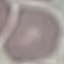
malaria_status: uninfected
image_type: automatically extracted cell patch, resized to 64 × 64 pixels
preparation: thin smear
capture: smartphone through the microscope eyepiece
stain: Giemsa